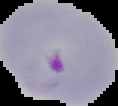
The area outside the segmented cell region is set to black. Image is 118×106 pixels. From a thin blood film. Result: malaria parasites identified.